Identify the parasite.
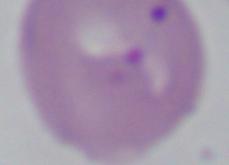

This is Babesia.

{
  "modality": "photomicrograph",
  "magnification": "1000x"
}